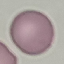
Summary:
  - Result: no malaria parasites seen
  - Image type: automatically extracted cell patch, resized to 64 × 64 pixels
  - Preparation: thin blood smear
  - Stain: Giemsa
  - Capture: smartphone camera at the microscope eyepiece